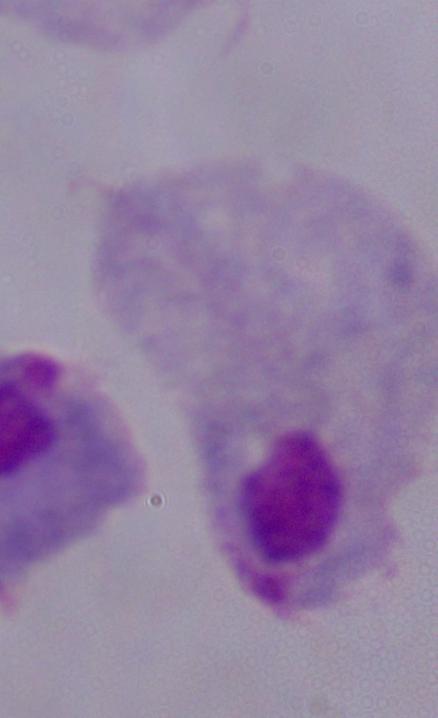

Summary:
  - Magnification: 1000x
  - Identification: trichomonad
  - Modality: photomicrograph